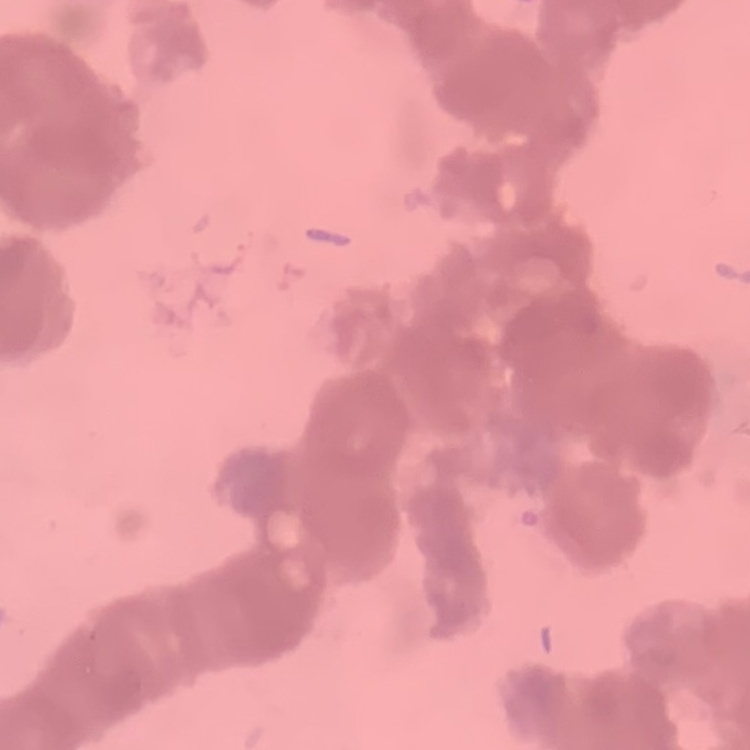
The erythrocytes exhibit rouleaux formation. One tile cut from a larger photomicrograph. Thin blood film. Stained with either Field's or Giemsa.